Assess the morphology of the erythrocytes.
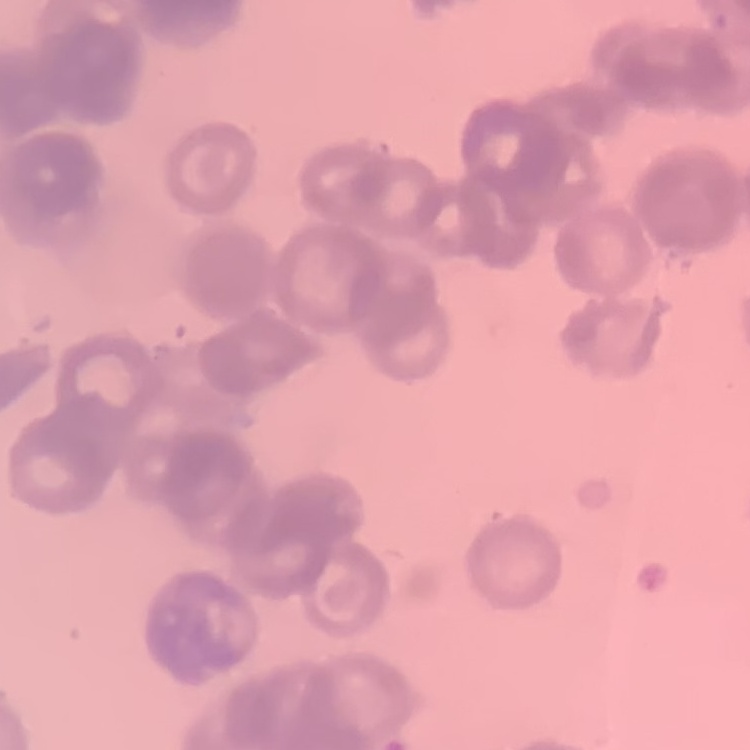
Rouleaux formation.

stain = Field's or Giemsa
image type = one tile cut from a larger photomicrograph
preparation = thin peripheral smear